Classify this cell by malaria status.
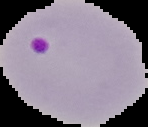
Parasitized.

{
  "image_size": "148×127 pixels",
  "image_type": "segmented cell region with the area outside set to black",
  "preparation": "thin blood smear"
}